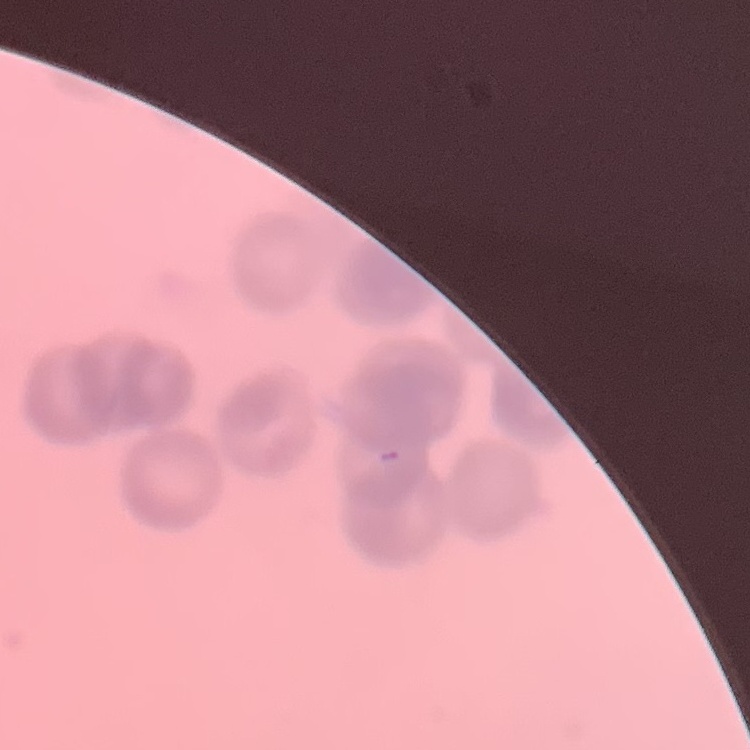
red_blood_cell_morphology: rouleaux formation
stain: Field's or Giemsa
image_type: one tile cut from a larger photomicrograph
preparation: thin blood smear